Locate and identify every blood parasite.
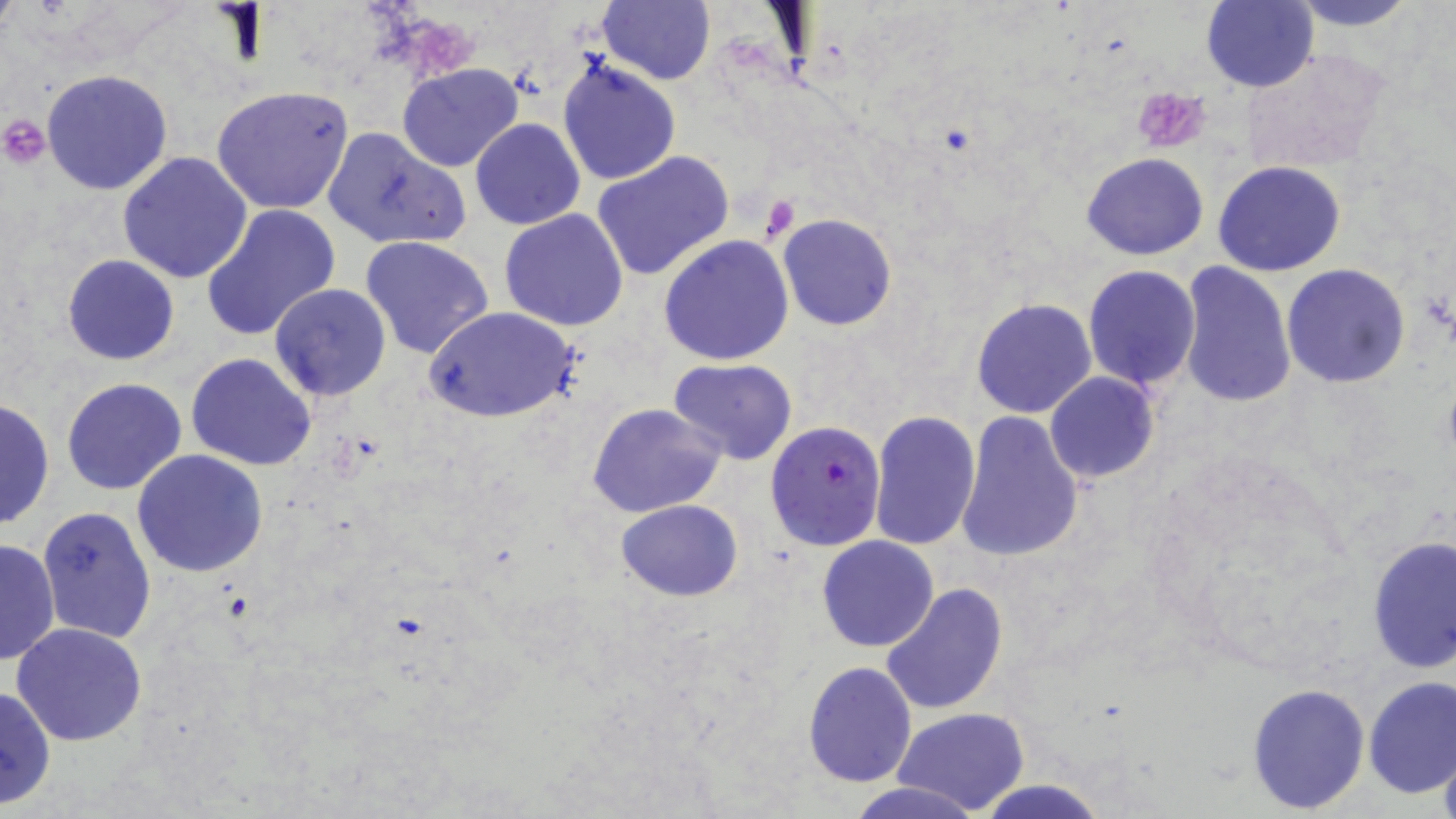
Approximate bounding boxes as named x1/y1/x2/y2 corners in pixels.
Plasmodium falciparum-infected red blood cells: (x1=764, y1=419, x2=885, y2=550).
No Plasmodium ovale, Plasmodium malariae, Plasmodium vivax, Babesia divergens, or Trypanosoma brucei observed.

Platelet locations: (x1=1131, y1=88, x2=1212, y2=153), (x1=1, y1=115, x2=50, y2=167), (x1=761, y1=192, x2=802, y2=240). Uninfected red blood cell locations: (x1=0, y1=0, x2=21, y2=39), (x1=596, y1=0, x2=717, y2=87), (x1=1287, y1=0, x2=1421, y2=30), (x1=1201, y1=1, x2=1318, y2=92), (x1=557, y1=56, x2=680, y2=187), (x1=396, y1=64, x2=524, y2=172), (x1=40, y1=69, x2=174, y2=194), (x1=212, y1=86, x2=354, y2=213), (x1=470, y1=117, x2=585, y2=230), (x1=320, y1=126, x2=471, y2=250), (x1=591, y1=150, x2=736, y2=284), (x1=1082, y1=151, x2=1209, y2=259), (x1=119, y1=152, x2=253, y2=284), (x1=1213, y1=161, x2=1348, y2=277), (x1=201, y1=204, x2=340, y2=341), (x1=499, y1=208, x2=630, y2=331), (x1=777, y1=213, x2=898, y2=331), (x1=659, y1=235, x2=795, y2=365), (x1=360, y1=236, x2=495, y2=359), (x1=62, y1=253, x2=180, y2=365), (x1=1177, y1=261, x2=1296, y2=409), (x1=1081, y1=264, x2=1201, y2=391), (x1=1281, y1=264, x2=1411, y2=389), (x1=268, y1=284, x2=393, y2=402), (x1=971, y1=298, x2=1097, y2=419), (x1=426, y1=307, x2=580, y2=423), (x1=186, y1=353, x2=316, y2=471), (x1=668, y1=357, x2=799, y2=466), (x1=1044, y1=372, x2=1161, y2=483), (x1=62, y1=378, x2=186, y2=495), (x1=0, y1=395, x2=55, y2=532), (x1=586, y1=401, x2=726, y2=519), (x1=868, y1=410, x2=981, y2=551), (x1=954, y1=410, x2=1085, y2=564), (x1=131, y1=451, x2=268, y2=578), (x1=616, y1=499, x2=742, y2=600), (x1=38, y1=505, x2=158, y2=644), (x1=1366, y1=535, x2=1454, y2=672), (x1=816, y1=536, x2=939, y2=653), (x1=1, y1=537, x2=59, y2=669), (x1=880, y1=582, x2=1007, y2=716), (x1=10, y1=623, x2=149, y2=747), (x1=802, y1=661, x2=917, y2=787), (x1=1362, y1=674, x2=1456, y2=801), (x1=1245, y1=681, x2=1370, y2=814), (x1=0, y1=686, x2=57, y2=809), (x1=894, y1=708, x2=1030, y2=815), (x1=1437, y1=744, x2=1456, y2=819), (x1=848, y1=780, x2=983, y2=819), (x1=977, y1=780, x2=1108, y2=819). Slide-level diagnosis: Plasmodium falciparum. Single field of view. May-Grünwald-Giemsa-stained preparation. Captured at 1000x magnification. Thin blood film. Light microscopy. Image is 1456×819 pixels.